Classify this cell by malaria status.
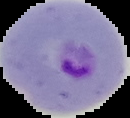

Parasitized.

Summary:
  - Image type: segmented cell region on a black background
  - Preparation: thin blood smear
  - Image size: 130×118 pixels